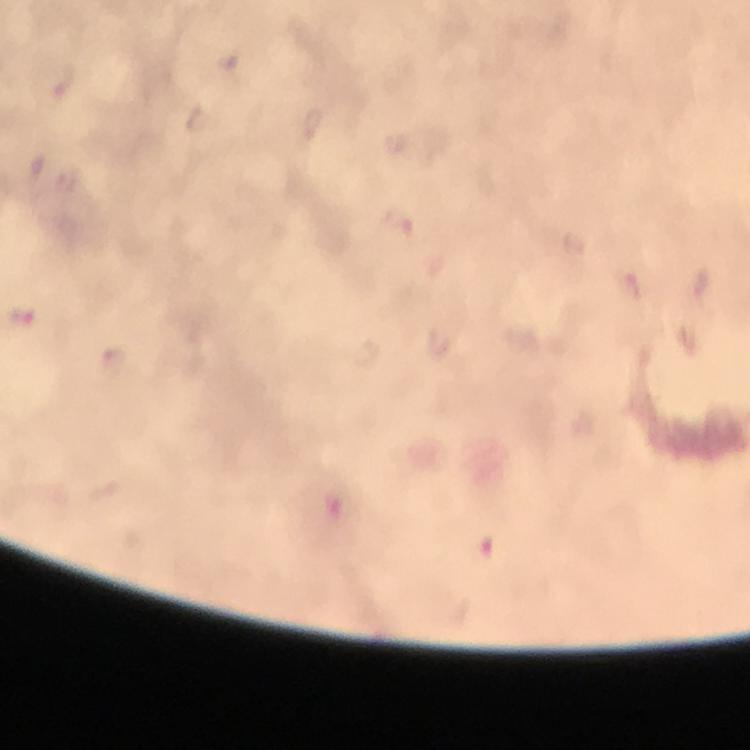

Approximate centers as [x, y] in pixels. Plasmodium parasite locations: [22, 317]. Immersion oil applied. Photographed through the microscope with a smartphone camera. Giemsa-stained preparation. From a diagnostic examination for malaria. At 100x magnification. Image is 750×750 pixels. Cropped region of a single field of view. Thick blood smear.